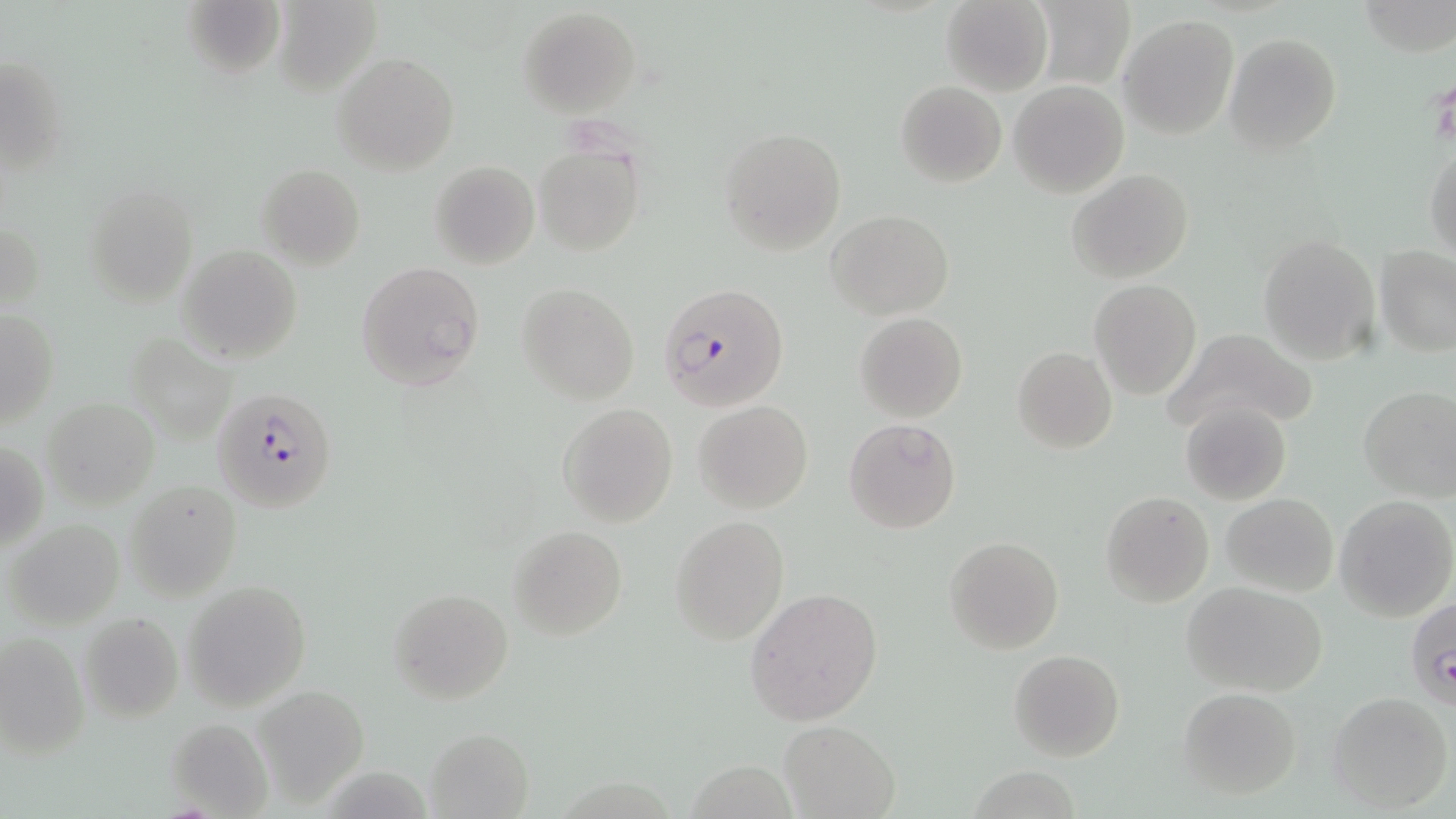
Summary:
  - Coordinate format: approximate bounding boxes as named x1/y1/x2/y2 corners in pixels
  - Plasmodium falciparum-infected red blood cell locations: (x1=657, y1=281, x2=788, y2=411), (x1=214, y1=387, x2=337, y2=511), (x1=1406, y1=599, x2=1456, y2=710)
  - Platelet locations: (x1=1428, y1=76, x2=1455, y2=146)
  - Uninfected red blood cell locations: (x1=179, y1=0, x2=285, y2=83), (x1=942, y1=0, x2=1052, y2=94), (x1=1030, y1=0, x2=1136, y2=89), (x1=271, y1=3, x2=380, y2=94), (x1=517, y1=6, x2=641, y2=117), (x1=1120, y1=14, x2=1238, y2=139), (x1=1224, y1=33, x2=1341, y2=155), (x1=2, y1=51, x2=67, y2=175), (x1=332, y1=52, x2=460, y2=175), (x1=896, y1=81, x2=1006, y2=187), (x1=1008, y1=81, x2=1129, y2=199), (x1=718, y1=126, x2=846, y2=254), (x1=1424, y1=142, x2=1456, y2=261), (x1=534, y1=143, x2=644, y2=258), (x1=429, y1=160, x2=540, y2=268), (x1=256, y1=162, x2=366, y2=269), (x1=1067, y1=168, x2=1194, y2=283), (x1=83, y1=182, x2=196, y2=304), (x1=827, y1=209, x2=953, y2=319), (x1=0, y1=216, x2=45, y2=315), (x1=1258, y1=234, x2=1382, y2=364), (x1=177, y1=246, x2=303, y2=364), (x1=1375, y1=247, x2=1456, y2=358), (x1=357, y1=261, x2=485, y2=391), (x1=1090, y1=279, x2=1201, y2=399), (x1=516, y1=283, x2=640, y2=403), (x1=0, y1=308, x2=59, y2=429), (x1=854, y1=313, x2=967, y2=423), (x1=1160, y1=328, x2=1317, y2=436), (x1=123, y1=332, x2=238, y2=440), (x1=1012, y1=345, x2=1118, y2=453), (x1=1357, y1=386, x2=1456, y2=500), (x1=43, y1=397, x2=158, y2=510), (x1=693, y1=400, x2=813, y2=513), (x1=1178, y1=400, x2=1291, y2=507), (x1=556, y1=403, x2=680, y2=527), (x1=842, y1=417, x2=961, y2=533), (x1=1, y1=436, x2=47, y2=554), (x1=124, y1=479, x2=243, y2=601), (x1=1100, y1=491, x2=1214, y2=606), (x1=1221, y1=492, x2=1340, y2=596), (x1=1335, y1=495, x2=1456, y2=620), (x1=670, y1=515, x2=788, y2=645), (x1=5, y1=519, x2=125, y2=631), (x1=507, y1=526, x2=628, y2=641), (x1=944, y1=536, x2=1063, y2=654), (x1=180, y1=579, x2=311, y2=710), (x1=1184, y1=581, x2=1327, y2=696), (x1=387, y1=587, x2=513, y2=705), (x1=746, y1=588, x2=883, y2=727), (x1=78, y1=612, x2=184, y2=723), (x1=0, y1=631, x2=90, y2=757), (x1=1009, y1=649, x2=1125, y2=762), (x1=254, y1=686, x2=371, y2=806), (x1=1176, y1=687, x2=1302, y2=799), (x1=1326, y1=691, x2=1452, y2=813), (x1=166, y1=717, x2=273, y2=819), (x1=779, y1=721, x2=899, y2=817), (x1=427, y1=727, x2=533, y2=817), (x1=967, y1=767, x2=1085, y2=818)
  - Slide-level diagnosis: Plasmodium falciparum
  - Modality: optical microscopy
  - Preparation: thin blood smear
  - Magnification: 1000x
  - Field of view: one of a larger specimen
  - Stain: May-Grünwald-Giemsa
  - Image size: 1456×819 pixels